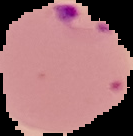

image size = 133×136 pixels
preparation = thin blood film
image type = segmented cell region with the area outside set to black
malaria status = parasitized